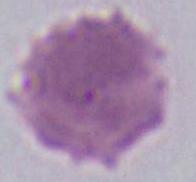
Summary:
  - Magnification: 1000x
  - Identification: erythrocyte
  - Modality: micrograph